Identify the blood parasite species.
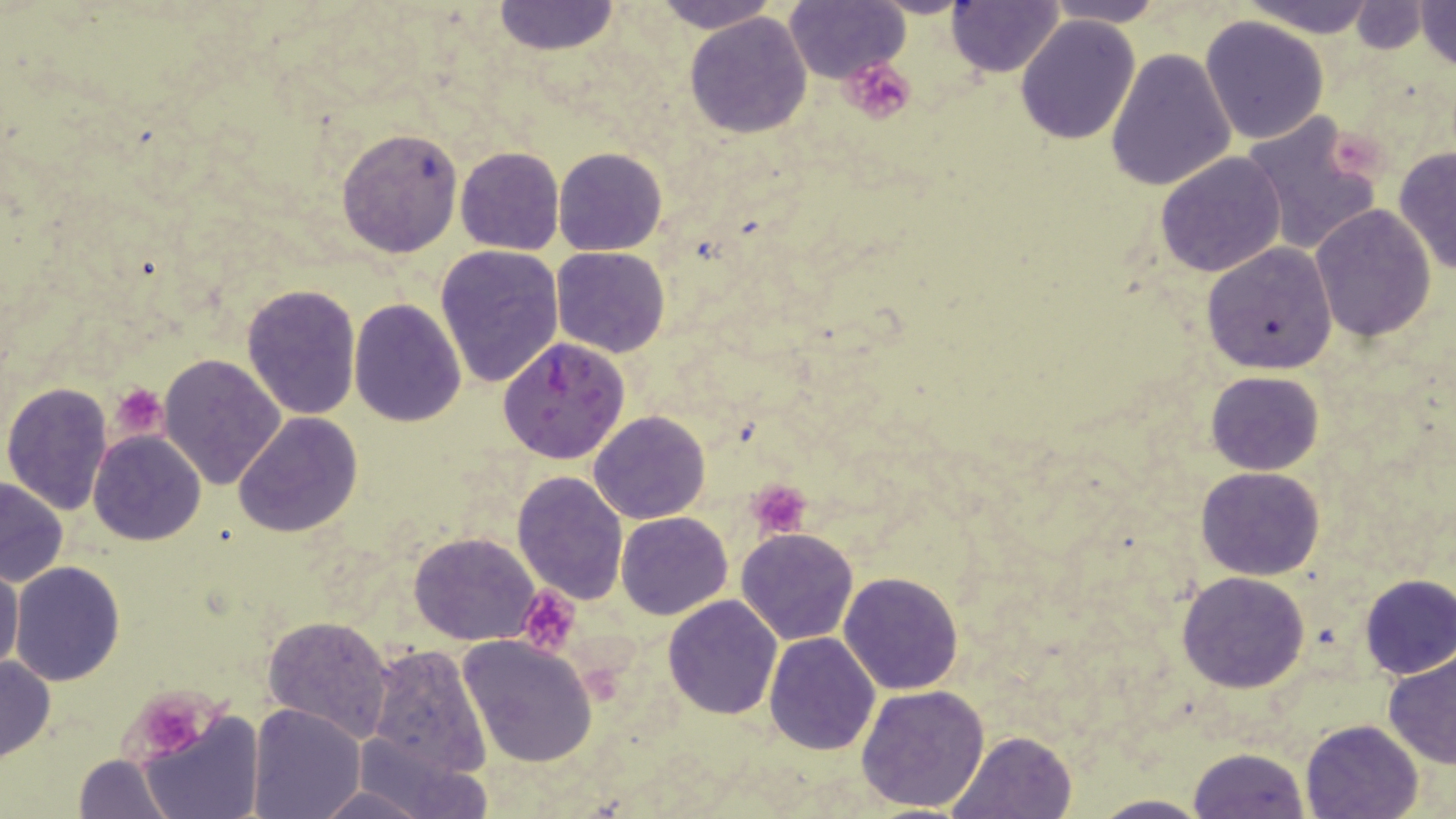
Plasmodium falciparum.

preparation = thin blood film
image size = 1456×819 pixels
modality = light microscopy
stain = May-Grünwald-Giemsa
magnification = 1000x
platelet locations = approximate bounding boxes as (x1, y1, x2, y2) in pixels: (841, 57, 918, 126), (1331, 133, 1384, 189), (108, 383, 168, 438), (746, 479, 811, 540), (516, 586, 582, 656), (134, 693, 208, 759)
Plasmodium falciparum-infected red blood cell locations = approximate bounding boxes as (x1, y1, x2, y2) in pixels: (498, 336, 630, 464)
field of view = single
uninfected red blood cell locations = approximate bounding boxes as (x1, y1, x2, y2) in pixels: (647, 0, 785, 31), (1042, 0, 1169, 26), (1238, 0, 1381, 35), (1413, 0, 1456, 71), (786, 1, 908, 84), (946, 1, 1065, 75), (491, 2, 621, 56), (1346, 4, 1432, 53), (685, 11, 813, 138), (1200, 15, 1329, 145), (1015, 16, 1140, 144), (1105, 46, 1238, 192), (1240, 112, 1387, 257), (337, 127, 462, 257), (553, 146, 667, 256), (1393, 146, 1456, 275), (456, 147, 564, 255), (1156, 151, 1288, 277), (1309, 206, 1436, 341), (1200, 242, 1339, 375), (436, 244, 564, 388), (553, 247, 669, 357), (241, 284, 361, 419), (348, 299, 467, 426), (158, 352, 286, 488), (1205, 371, 1324, 475), (2, 381, 114, 515), (589, 411, 710, 524), (233, 413, 364, 537), (546, 414, 677, 552), (89, 429, 207, 545), (1195, 465, 1324, 581), (512, 470, 629, 605), (0, 478, 70, 588), (616, 512, 733, 621), (735, 527, 858, 645), (407, 531, 543, 646), (10, 561, 126, 686), (0, 563, 25, 676), (1176, 571, 1310, 694), (839, 572, 964, 695), (1358, 575, 1456, 680), (662, 593, 783, 720), (263, 614, 395, 741), (764, 631, 881, 754), (457, 635, 598, 767), (364, 645, 492, 779), (1382, 653, 1456, 769), (0, 655, 55, 760), (855, 683, 990, 814), (247, 703, 364, 818), (139, 710, 262, 819), (1300, 718, 1424, 819), (350, 728, 491, 818), (948, 731, 1078, 819), (1190, 747, 1309, 818), (74, 753, 177, 818), (309, 785, 445, 817), (1089, 794, 1212, 818)